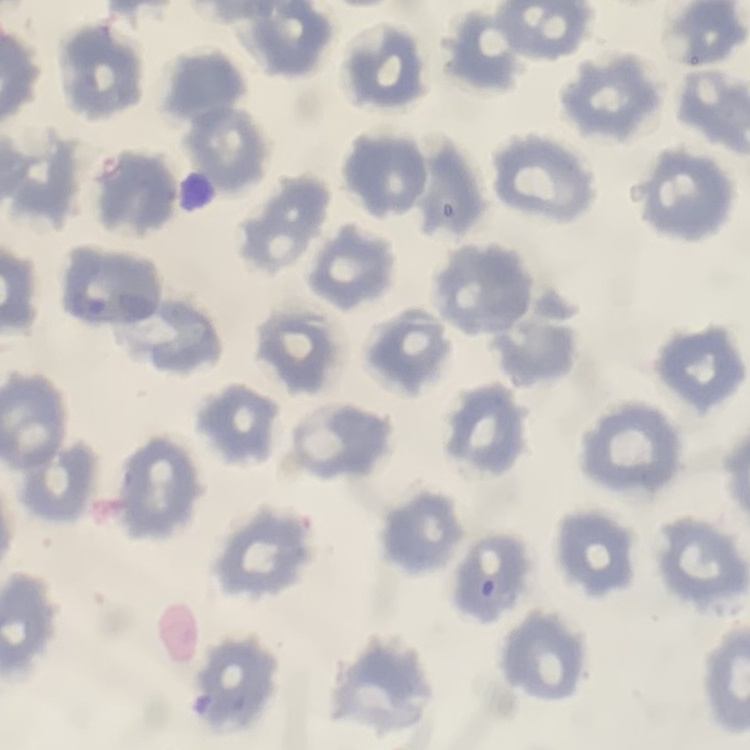

red blood cell morphology = no rouleaux formation
stain = Field's or Giemsa
image type = square crop of a larger photomicrograph
preparation = thin blood film